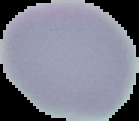
Result: negative for Plasmodium parasites. From a thin blood film. Segmented cell region on a black background. Image is 139×121 pixels.